Classify this cell by malaria status.
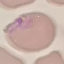
Parasitized.

Summary:
  - Capture: smartphone through the microscope eyepiece
  - Stain: Giemsa
  - Image type: cell patch, automatically extracted from a larger field of view and resized to 64 × 64 pixels
  - Preparation: thin smear